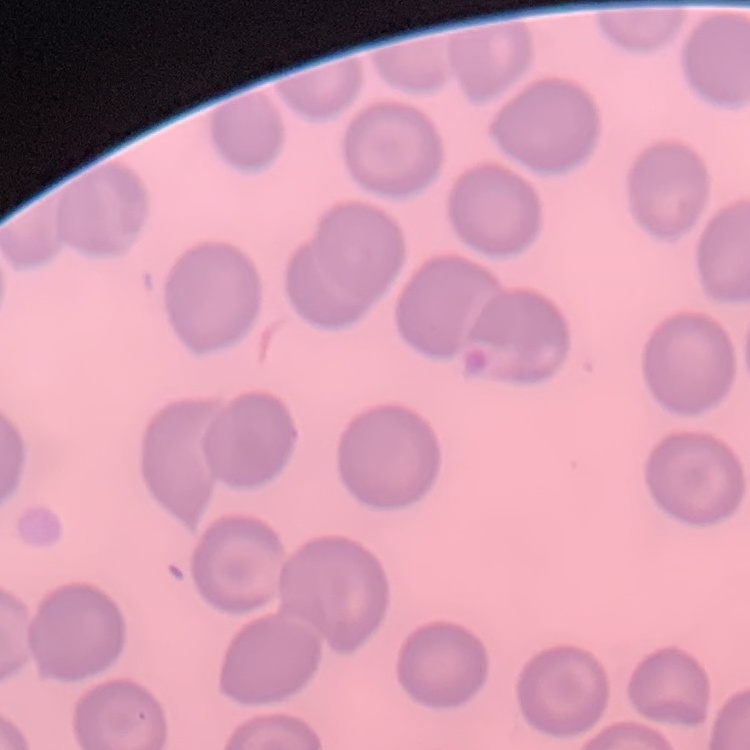

red blood cell morphology = no rouleaux formation
preparation = thin blood smear
stain = Field's or Giemsa
image type = one tile cut from a larger photomicrograph